Assess the morphology of the red blood cells.
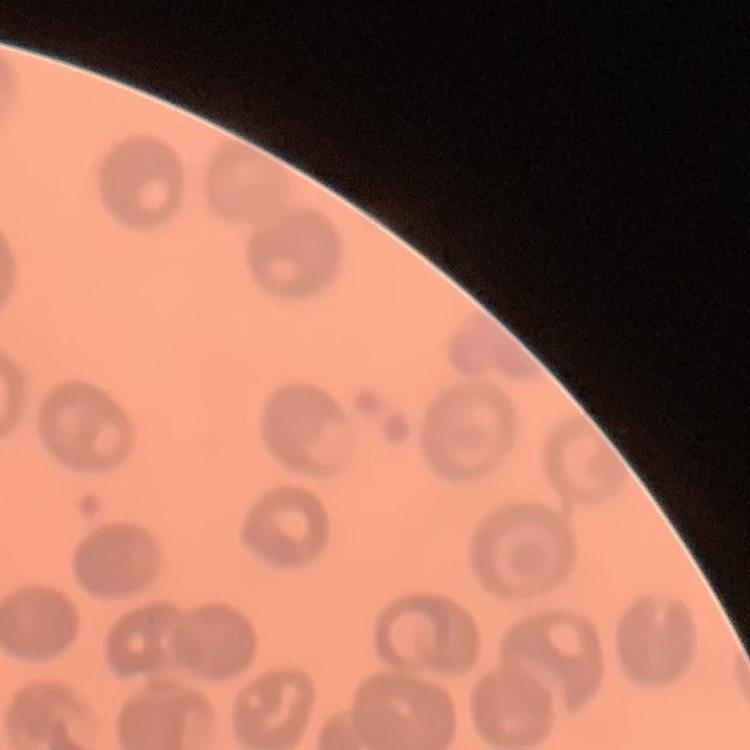

They show no rouleaux formation.

stain = Field's or Giemsa
image type = one tile cut from a larger photomicrograph
preparation = thin blood smear